Comment on the morphology of the erythrocytes.
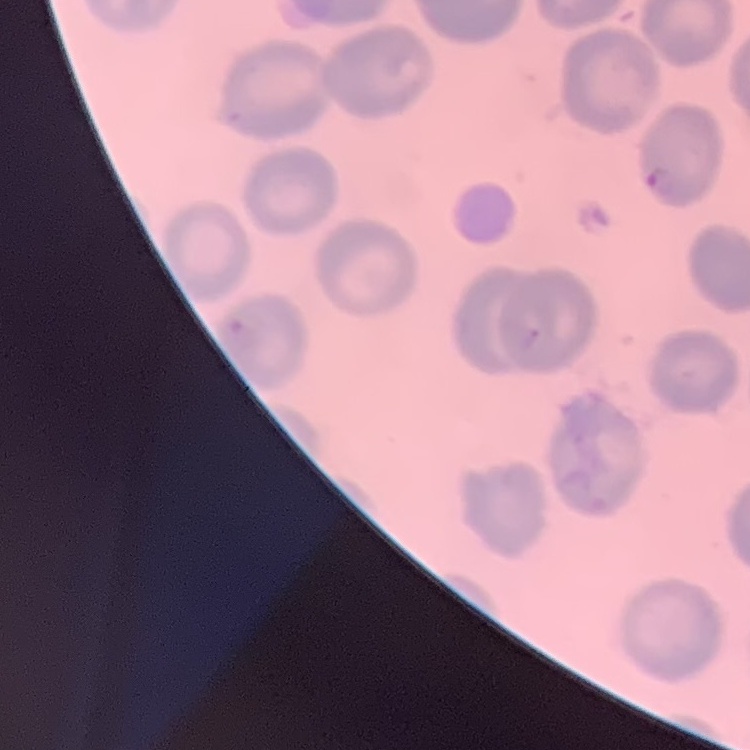
They show no rouleaux formation.

stain = Field's or Giemsa
preparation = thin blood smear
image type = one tile cut from a larger photomicrograph